State which parasite is depicted.
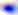

This is Toxoplasma gondii.

magnification: 400x
modality: micrograph